Name the parasite shown.
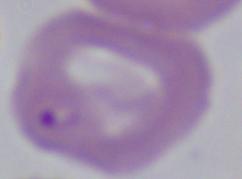

Babesia.

Photomicrograph. 1000x magnification.